Assess this cell for malaria.
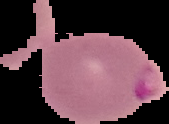
Parasitized.

From a thin blood smear. Image is 169×124 pixels. The area outside the segmented cell region is set to black.